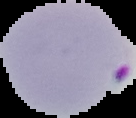

image type = segmented cell region with the area outside set to black
image size = 136×118 pixels
preparation = thin blood smear
result = Plasmodium parasites identified